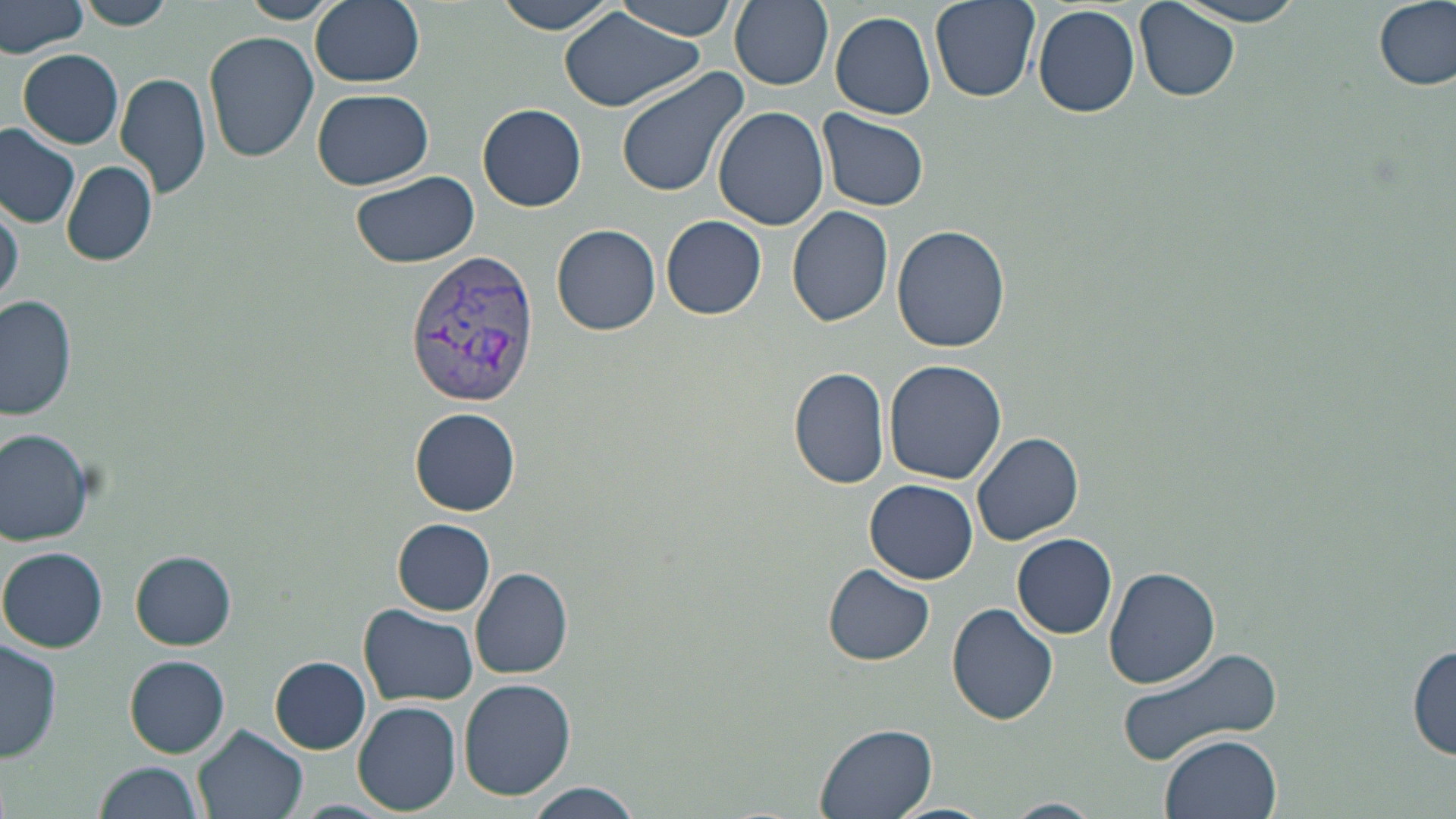
Summary:
  - Coordinate format: approximate bounding boxes as (x1, y1, x2, y2) in pixels
  - Uninfected red blood cell locations: (236, 0, 339, 23), (311, 0, 424, 88), (497, 0, 621, 37), (612, 0, 738, 40), (730, 0, 834, 89), (929, 0, 1041, 103), (1171, 0, 1313, 26), (1374, 0, 1455, 91), (0, 1, 90, 57), (78, 1, 174, 30), (1136, 3, 1241, 103), (1032, 4, 1140, 118), (558, 6, 704, 114), (830, 11, 937, 120), (204, 30, 320, 162), (19, 50, 125, 147), (615, 65, 749, 198), (116, 71, 212, 199), (311, 88, 434, 190), (478, 104, 587, 211), (714, 105, 829, 231), (818, 111, 930, 212), (0, 127, 79, 229), (60, 162, 158, 265), (349, 169, 478, 269), (1, 194, 22, 310), (786, 204, 894, 326), (662, 215, 767, 319), (552, 223, 661, 335), (892, 225, 1011, 354), (2, 296, 78, 420), (883, 358, 1007, 485), (789, 366, 892, 489), (410, 407, 518, 515), (0, 427, 97, 546), (972, 432, 1083, 546), (866, 479, 979, 583), (393, 519, 497, 615), (1011, 533, 1118, 639), (1, 546, 107, 652), (130, 550, 236, 650), (823, 565, 935, 665), (470, 566, 574, 679), (1104, 566, 1221, 690), (947, 603, 1059, 725), (361, 604, 479, 706), (1, 636, 62, 763), (1118, 643, 1286, 765), (1408, 643, 1455, 762), (126, 656, 231, 758), (270, 657, 371, 754), (459, 678, 576, 802), (353, 702, 460, 816), (194, 723, 307, 819), (813, 723, 939, 819), (1161, 733, 1280, 819), (94, 760, 206, 819), (518, 781, 646, 819), (998, 798, 1102, 819), (882, 802, 996, 819)
  - Plasmodium vivax-infected red blood cell locations: (405, 248, 541, 406)
  - Slide-level diagnosis: Plasmodium vivax
  - Field of view: single
  - Image size: 1456×819 pixels
  - Preparation: thin blood smear
  - Magnification: 1000x
  - Modality: light microscopy
  - Stain: May-Grünwald-Giemsa